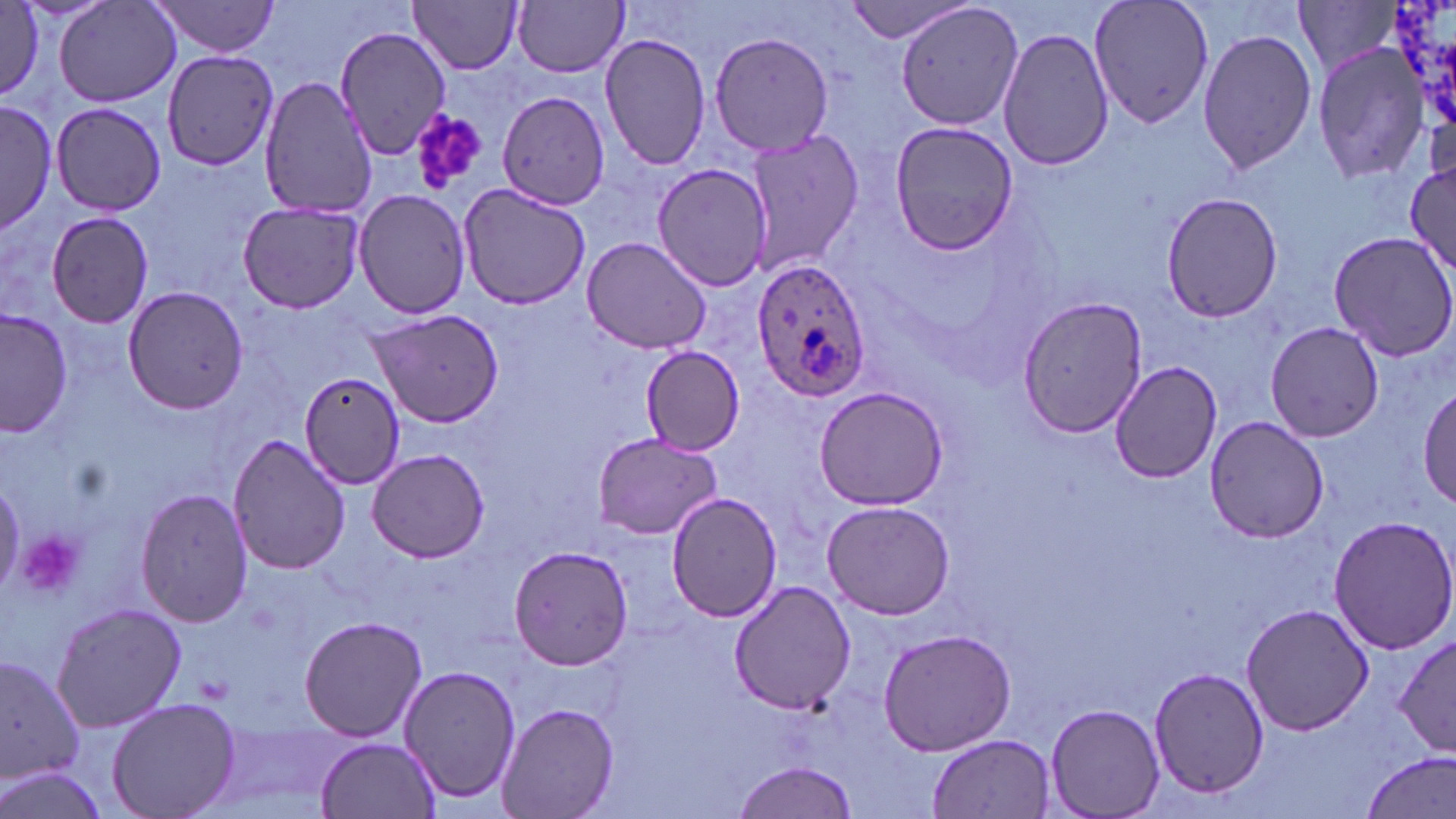

slide-level diagnosis = Plasmodium ovale
image size = 1456×819 pixels
platelet locations = approximate bounding boxes as (x1,y1)-(x2,y2) corner pairs in pixels: (410,108)-(488,193), (17,531)-(86,601)
preparation = thin blood film
Plasmodium ovale-infected red blood cell locations = approximate bounding boxes as (x1,y1)-(x2,y2) corner pairs in pixels: (750,256)-(875,399)
modality = optical microscopy
magnification = 1000x
uninfected red blood cell locations = approximate bounding boxes as (x1,y1)-(x2,y2) corner pairs in pixels: (149,0)-(286,59), (514,0)-(628,78), (842,0)-(975,44), (895,0)-(1024,132), (1088,0)-(1214,130), (1387,0)-(1454,132), (53,1)-(182,108), (409,1)-(524,74), (1293,1)-(1398,77), (0,3)-(50,105), (998,25)-(1115,173), (333,26)-(451,160), (1197,26)-(1319,177), (710,31)-(837,158), (599,32)-(713,173), (1312,46)-(1429,183), (163,50)-(280,176), (495,75)-(610,214), (259,77)-(379,217), (0,98)-(58,234), (50,101)-(168,216), (888,122)-(1020,255), (744,127)-(863,272), (1406,156)-(1454,276), (653,162)-(776,291), (457,184)-(591,310), (354,190)-(472,318), (1160,191)-(1286,323), (237,202)-(365,313), (45,211)-(154,329), (1327,231)-(1456,359), (579,235)-(711,353), (121,285)-(251,414), (1016,295)-(1148,437), (1,309)-(73,437), (365,310)-(504,426), (1264,321)-(1384,442), (641,348)-(746,454), (1108,359)-(1225,482), (300,370)-(407,490), (813,386)-(952,511), (1418,386)-(1455,511), (1204,416)-(1329,542), (591,431)-(724,539), (228,433)-(350,576), (368,448)-(489,563), (133,487)-(254,628), (667,490)-(782,623), (820,499)-(956,620), (1325,514)-(1456,655), (503,543)-(636,671), (728,580)-(855,715), (51,603)-(187,732), (1241,603)-(1373,737), (298,613)-(429,741), (878,628)-(1018,756), (1392,633)-(1456,757), (1,651)-(84,793), (399,663)-(521,805), (1147,666)-(1270,800), (105,697)-(241,819), (495,702)-(618,818), (1045,703)-(1166,818), (928,733)-(1055,816), (316,736)-(440,818), (1361,752)-(1455,819), (732,760)-(857,819), (0,764)-(114,818)
stain = May-Grünwald-Giemsa
field of view = single